Assess this cell for malaria.
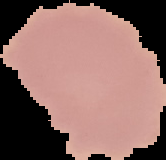
Uninfected.

Summary:
  - Preparation: thin blood smear
  - Image size: 166×160 pixels
  - Image type: cell region segmented out of the field of view; surrounding area masked to black